Report the malaria status of this cell.
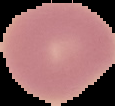
Uninfected.

Segmented cell region on a black background. Image is 115×106 pixels. From a thin blood smear.